Locate every blood parasite and identify its species.
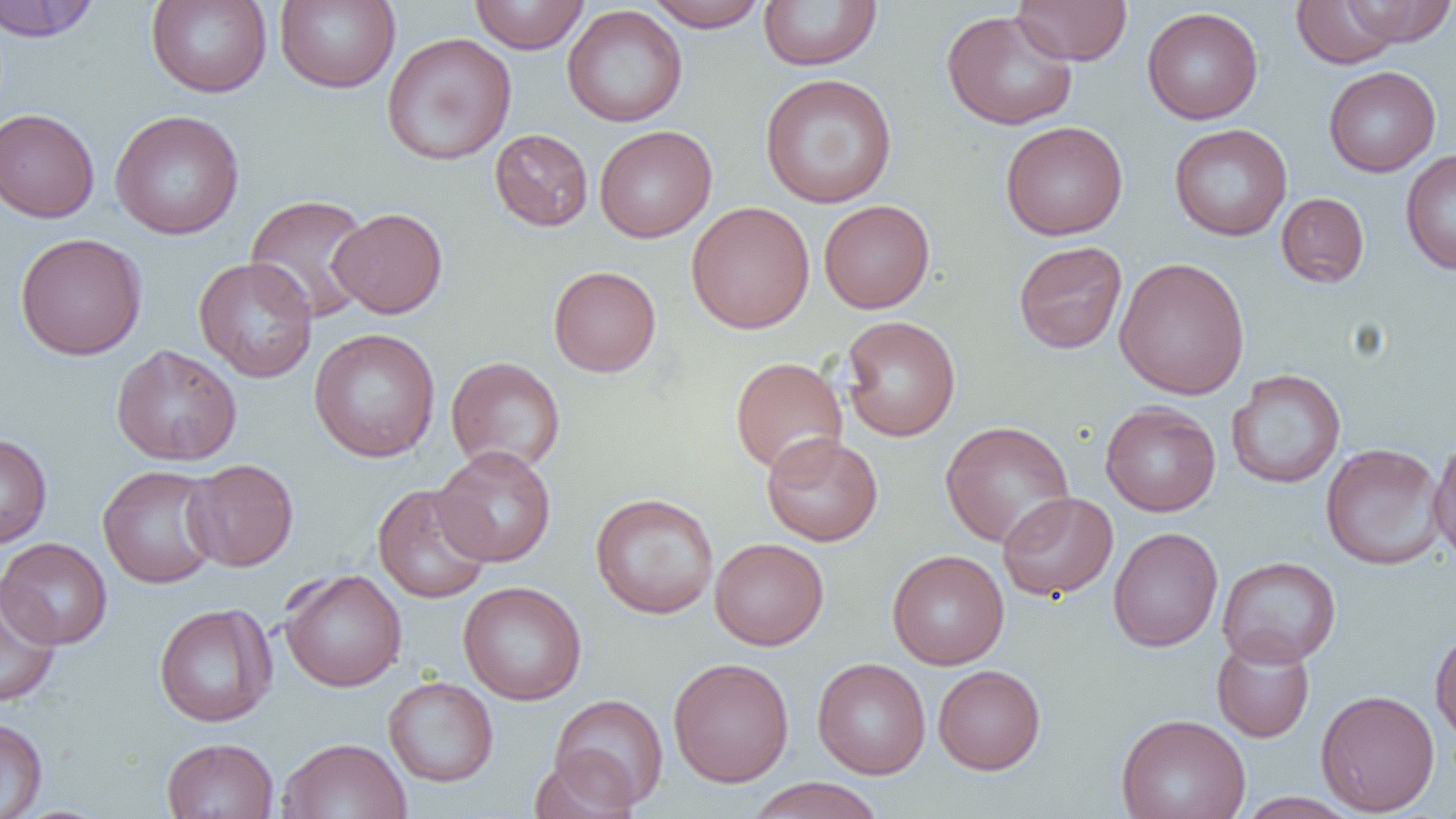
No blood parasites observed.

Approximate bounding boxes as [x1, y1, x2, y2] in pixels. Uninfected red blood cell locations: [0, 0, 102, 42], [146, 0, 272, 98], [274, 0, 400, 93], [469, 0, 589, 54], [644, 0, 769, 32], [759, 0, 882, 71], [1012, 0, 1131, 65], [1290, 0, 1406, 69], [1339, 0, 1456, 47], [562, 5, 688, 127], [1142, 7, 1263, 124], [940, 9, 1078, 131], [382, 32, 517, 165], [1323, 66, 1440, 177], [759, 73, 898, 208], [0, 108, 99, 222], [109, 109, 245, 240], [1000, 121, 1128, 240], [1169, 123, 1292, 241], [594, 125, 717, 243], [489, 129, 593, 232], [1400, 149, 1456, 275], [1276, 192, 1369, 287], [244, 194, 375, 325], [819, 199, 935, 313], [686, 201, 814, 334], [329, 207, 447, 318], [14, 232, 147, 360], [1013, 241, 1128, 354], [193, 257, 318, 382], [1113, 257, 1250, 400], [548, 265, 661, 377], [839, 315, 961, 442], [309, 328, 440, 462], [111, 344, 242, 466], [446, 356, 566, 474], [730, 356, 847, 475], [1226, 369, 1346, 489], [1099, 402, 1221, 516], [939, 420, 1076, 548], [762, 432, 883, 546], [0, 433, 52, 548], [1428, 436, 1456, 566], [1320, 442, 1447, 570], [432, 445, 556, 567], [183, 459, 299, 572], [97, 464, 223, 589], [373, 483, 493, 603], [590, 492, 719, 619], [997, 492, 1118, 601], [1108, 526, 1223, 652], [0, 537, 113, 649], [709, 537, 828, 650], [887, 550, 1009, 670], [1216, 556, 1342, 668], [279, 568, 407, 692], [0, 576, 62, 707], [458, 581, 587, 705], [154, 603, 277, 727], [1430, 625, 1456, 744], [1211, 635, 1315, 742], [668, 657, 794, 787], [812, 657, 931, 779], [932, 664, 1046, 774], [383, 676, 499, 787], [1315, 689, 1440, 816], [548, 694, 669, 811], [1116, 713, 1250, 819], [0, 717, 48, 819], [162, 737, 278, 818], [276, 737, 412, 819], [529, 752, 637, 819], [746, 777, 886, 819], [1236, 792, 1360, 819]. Slide-level diagnosis: no evidence of blood parasites. 1000x magnification. Image is 1456×819 pixels. Thin blood smear. Single field of view. Optical microscopy.